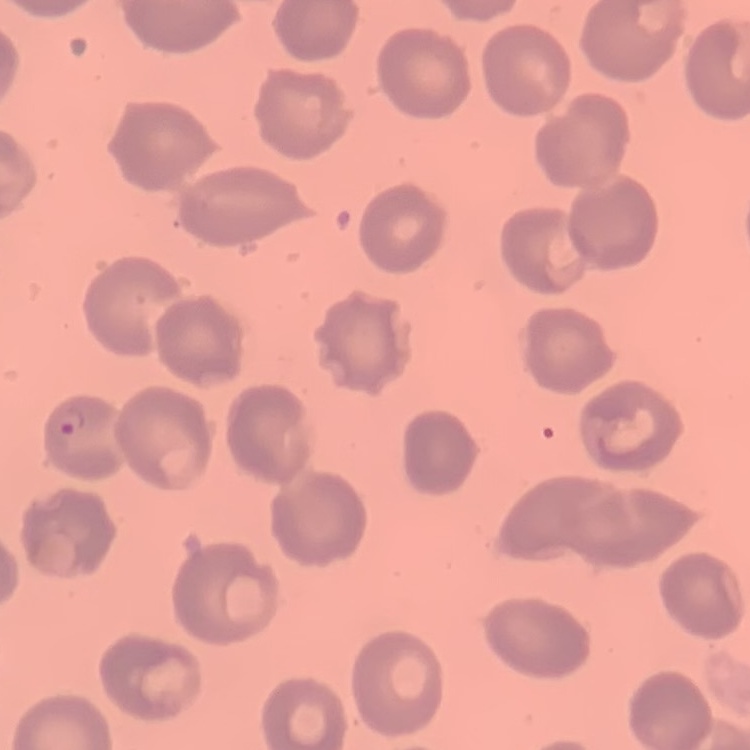
The erythrocytes exhibit no rouleaux formation. Thin blood film. One tile cut from a larger photomicrograph. Stained with either Field's or Giemsa.